Locate every Plasmodium malariae-infected red blood cell.
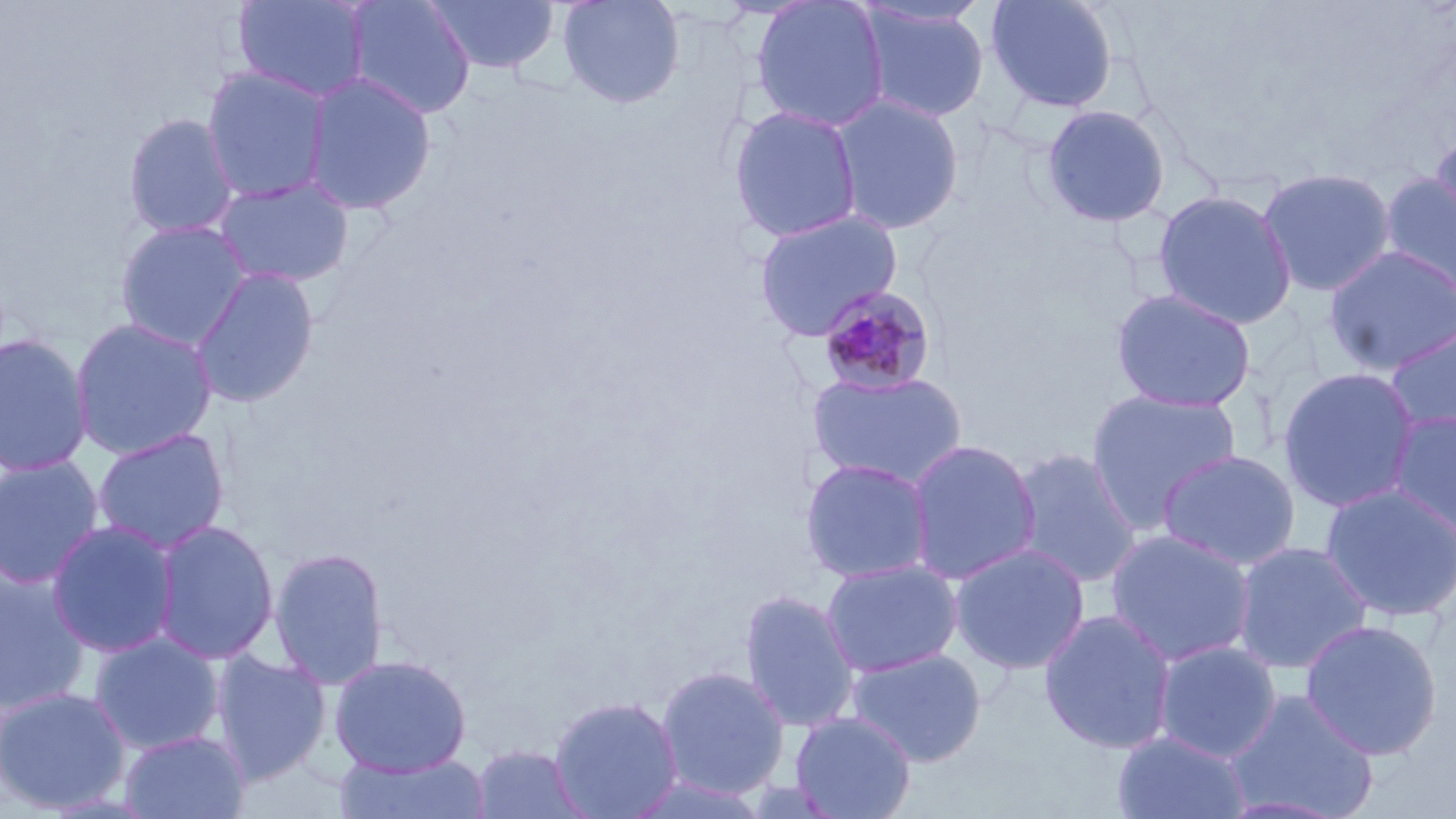
Approximate bounding boxes as (x1,y1)-(x2,y2) corner pairs in pixels.
Plasmodium malariae-infected red blood cells: (817,285)-(936,397).

Uninfected red blood cell locations: (233,0)-(372,103), (345,0)-(476,121), (423,0)-(560,74), (556,0)-(685,109), (749,0)-(891,133), (984,0)-(1120,115), (857,3)-(991,124), (201,66)-(333,204), (302,72)-(438,215), (830,93)-(965,236), (728,104)-(864,243), (1040,104)-(1171,229), (122,112)-(241,240), (1429,124)-(1456,241), (1257,166)-(1397,297), (1379,173)-(1456,303), (212,176)-(355,288), (1152,189)-(1297,330), (752,208)-(904,341), (114,220)-(254,350), (1323,245)-(1456,376), (189,265)-(320,408), (1110,288)-(1258,413), (69,317)-(218,459), (1384,324)-(1456,437), (0,332)-(94,476), (1277,367)-(1421,513), (806,369)-(969,490), (1085,388)-(1243,532), (1387,409)-(1456,540), (91,427)-(231,554), (905,438)-(1041,585), (1009,447)-(1143,588), (1156,449)-(1302,571), (0,454)-(106,590), (799,457)-(935,584), (1319,482)-(1456,622), (46,519)-(180,658), (152,519)-(280,664), (1105,528)-(1257,667), (1232,540)-(1374,674), (949,543)-(1090,675), (268,546)-(389,689), (820,558)-(963,677), (0,565)-(92,716), (738,589)-(861,734), (1038,609)-(1178,754), (1299,618)-(1443,760), (88,633)-(225,755), (1153,641)-(1282,762), (846,647)-(987,767), (211,650)-(331,785), (328,654)-(471,776), (655,665)-(790,799), (0,686)-(131,813), (1224,688)-(1380,819), (548,695)-(684,819), (790,711)-(917,819), (119,729)-(250,819), (1112,730)-(1251,819), (470,744)-(590,819), (334,751)-(490,819). Slide-level diagnosis: Plasmodium malariae. Image is 1456×819 pixels. May-Grünwald-Giemsa-stained preparation. 1000x magnification. Thin blood smear. One field of a larger specimen. Optical microscopy.